Report the malaria status.
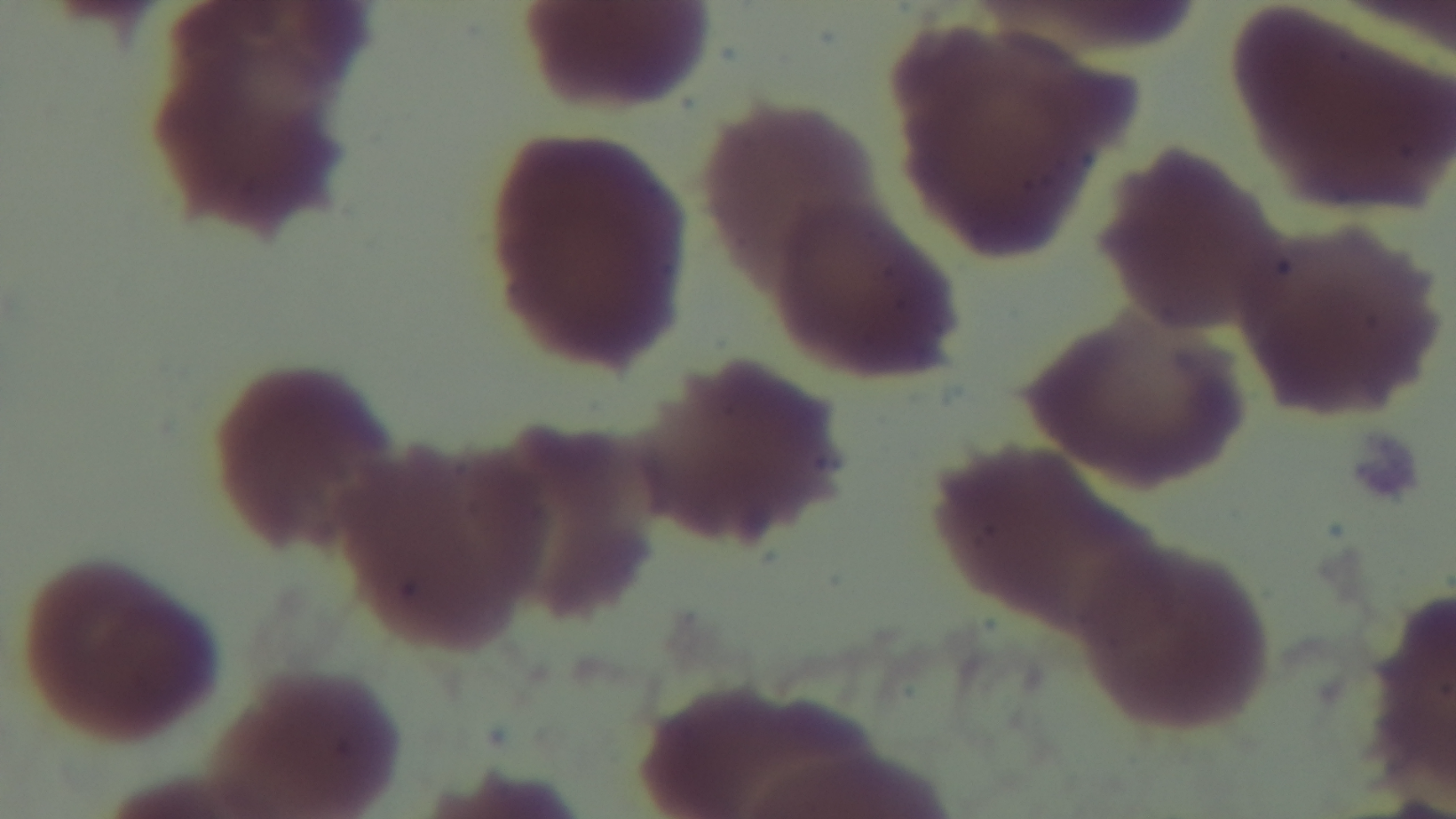

It is uninfected.

{
  "preparation": "thin",
  "field_of_view": "one from the slide",
  "modality": "light microscopy",
  "capture": "mounted 4K digital camera",
  "objective": "100x oil immersion",
  "stain": "Giemsa"
}